Outline each Plasmodium malariae-infected red blood cell.
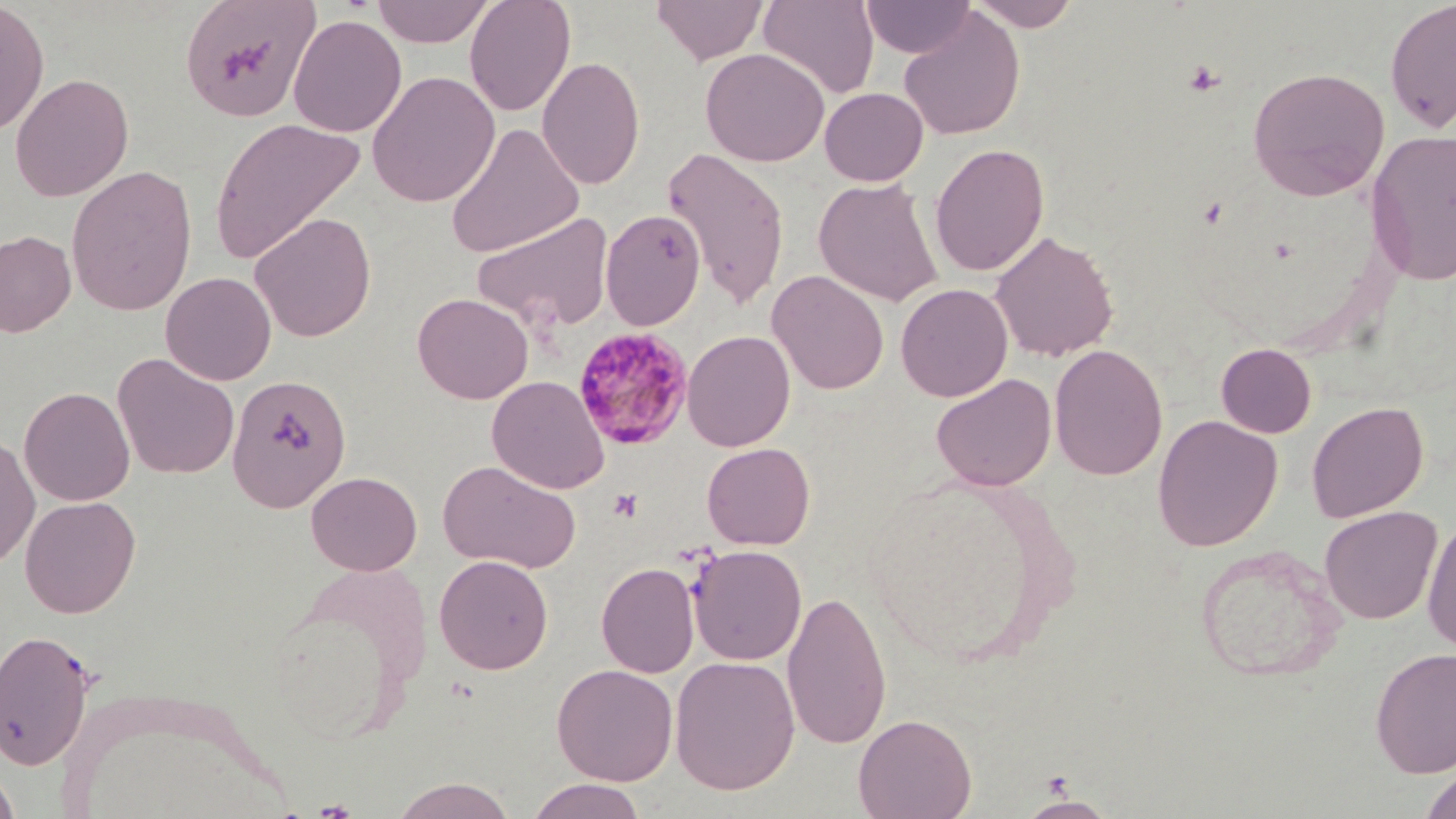
Approximate bounding boxes as [x1, y1, x2, y2] in pixels.
Plasmodium malariae-infected red blood cells: [572, 327, 694, 450].

slide-level diagnosis = Plasmodium malariae
field of view = single
image size = 1456×819 pixels
platelet locations = approximate bounding boxes as [x1, y1, x2, y2] in pixels: [1183, 61, 1225, 96], [608, 490, 642, 522]
preparation = thin blood smear
uninfected red blood cell locations = approximate bounding boxes as [x1, y1, x2, y2] in pixels: [179, 0, 321, 123], [371, 0, 495, 47], [464, 0, 576, 117], [651, 0, 769, 65], [758, 0, 879, 99], [860, 0, 975, 58], [968, 0, 1081, 31], [1385, 0, 1456, 133], [0, 1, 49, 136], [899, 8, 1025, 141], [288, 14, 406, 137], [700, 47, 830, 167], [537, 55, 645, 189], [1247, 66, 1390, 201], [366, 70, 501, 208], [9, 73, 134, 202], [819, 86, 928, 186], [209, 117, 365, 264], [445, 122, 585, 258], [1366, 129, 1456, 286], [929, 143, 1050, 277], [661, 146, 790, 310], [65, 164, 198, 316], [813, 178, 943, 305], [600, 209, 706, 330], [249, 212, 376, 341], [472, 213, 614, 332], [0, 229, 76, 338], [990, 230, 1119, 362], [767, 270, 888, 394], [160, 271, 276, 386], [895, 283, 1013, 401], [412, 292, 533, 404], [682, 330, 795, 452], [1049, 343, 1168, 481], [1216, 343, 1317, 438], [112, 353, 240, 480], [931, 373, 1056, 491], [227, 374, 351, 512], [486, 376, 610, 494], [19, 386, 135, 506], [1306, 401, 1429, 522], [1152, 415, 1283, 551], [0, 433, 40, 572], [701, 442, 815, 549], [438, 460, 581, 573], [305, 471, 422, 575], [19, 495, 141, 618], [1319, 505, 1442, 625], [1421, 517, 1456, 655], [688, 545, 807, 665], [1196, 545, 1344, 683], [434, 554, 554, 674], [596, 562, 699, 678], [781, 588, 891, 751], [0, 629, 98, 771], [1369, 648, 1456, 778], [670, 656, 800, 795], [551, 663, 678, 785], [853, 713, 977, 819], [0, 765, 20, 819], [1420, 768, 1456, 819], [389, 777, 518, 819], [525, 778, 649, 819], [1018, 795, 1117, 818]
modality = optical microscopy
magnification = 1000x
stain = May-Grünwald-Giemsa